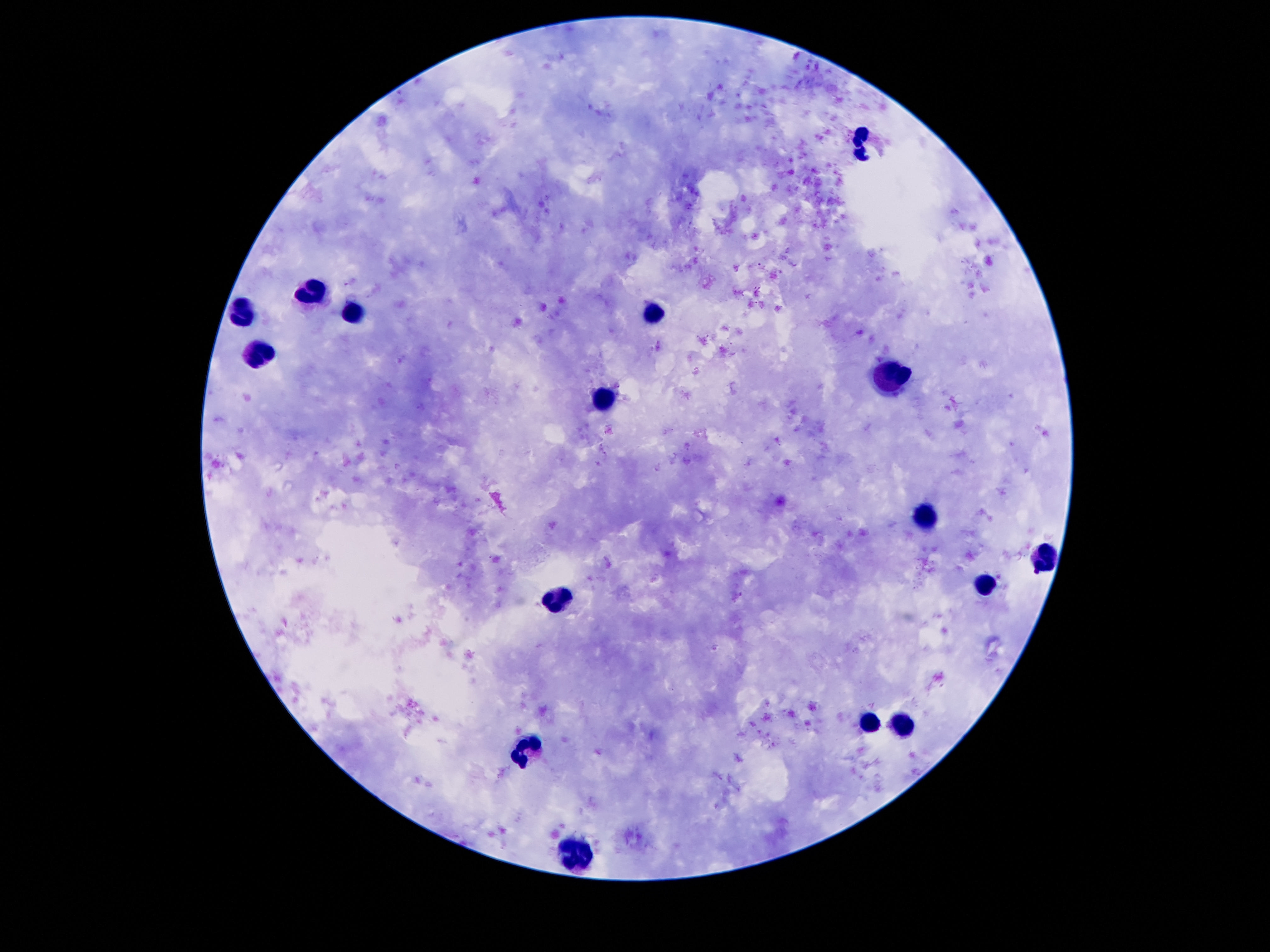

capture = smartphone camera through the microscope eyepiece
field of view = one from this slide
leukocyte locations = approximate centers as {x, y} in pixels: {864, 146}, {311, 292}, {353, 308}, {242, 310}, {656, 312}, {259, 354}, {897, 381}, {605, 399}, {927, 518}, {1044, 560}, {986, 586}, {557, 600}, {868, 722}, {899, 725}, {532, 749}, {576, 853}
preparation = thick blood smear
magnification = 100x
image size = 1270×952 pixels
patient malaria status = uninfected
stain = Giemsa